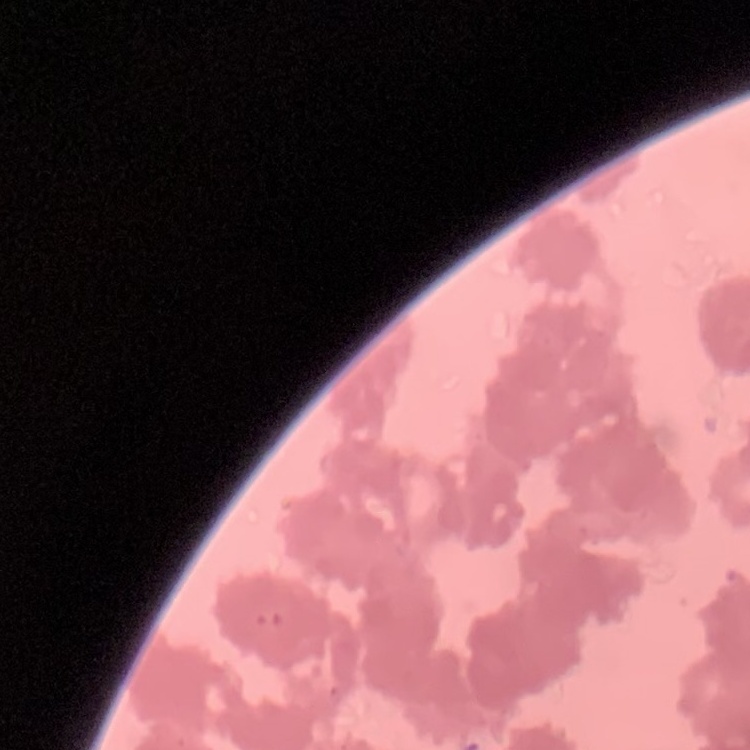

Summary:
  - Erythrocyte morphology: rouleaux formation
  - Stain: Field's or Giemsa
  - Preparation: thin blood film
  - Image type: one tile cut from a larger photomicrograph